Comment on the morphology of the erythrocytes.
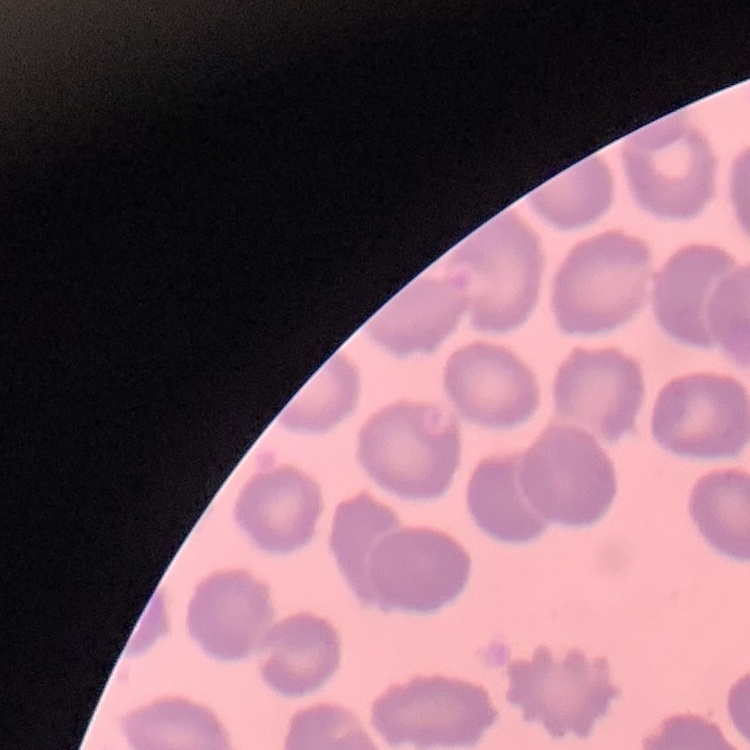
They show no rouleaux formation.

Thin blood smear. Square crop of a larger photomicrograph. Stained with either Field's or Giemsa.